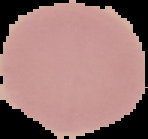

Summary:
  - Malaria status: uninfected
  - Image type: cell region segmented out of the field of view; surrounding area masked to black
  - Preparation: thin blood film
  - Image size: 148×139 pixels